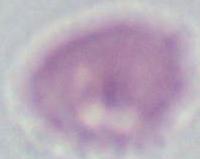
identification = erythrocyte
magnification = 1000x
modality = micrograph